Assess the morphology of the erythrocytes.
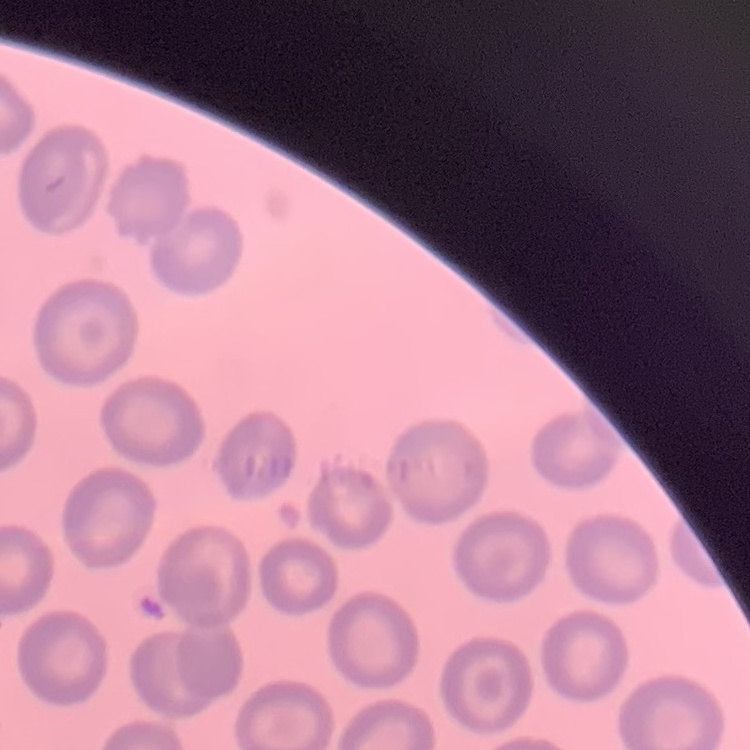
They show no rouleaux formation.

stain = Field's or Giemsa
preparation = thin blood smear
image type = one tile cut from a larger photomicrograph